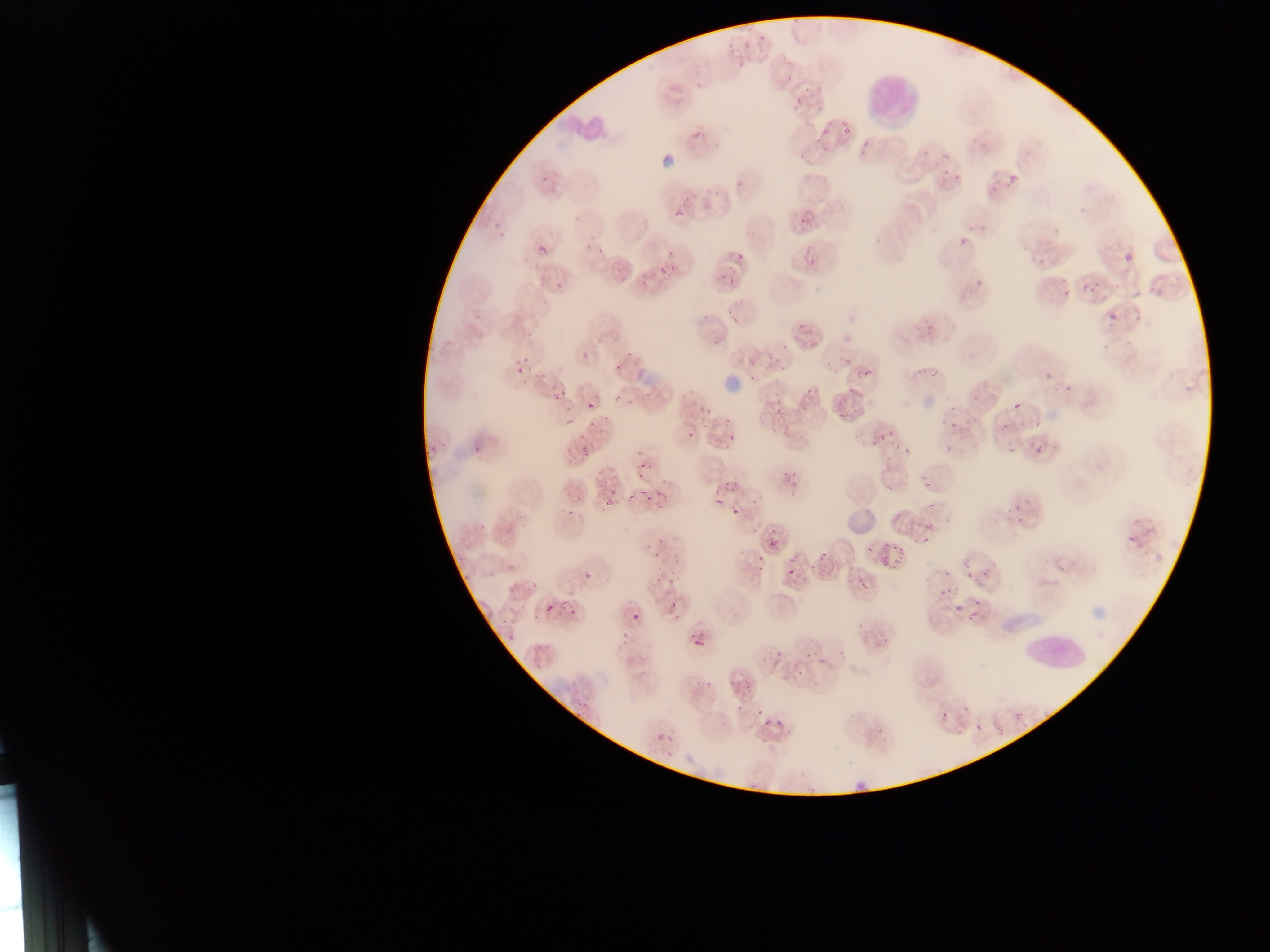
{
  "country": "Ghana",
  "field_of_view": "single",
  "leukocyte_locations": "approximate bounding boxes as {left, top, right, bottom} in pixels: {863, 62, 922, 128}, {545, 102, 611, 145}, {1021, 608, 1087, 678}",
  "malaria_parasite_locations": "approximate bounding boxes as {left, top, right, bottom} in pixels: {695, 83, 703, 91}, {692, 131, 702, 140}, {537, 174, 548, 181}, {1011, 175, 1018, 183}, {735, 180, 749, 189}, {683, 189, 697, 199}, {711, 189, 726, 200}, {699, 197, 713, 211}, {673, 203, 686, 220}, {1080, 207, 1087, 216}, {797, 209, 814, 224}, {486, 214, 505, 228}, {498, 227, 511, 239}, {957, 231, 970, 245}, {538, 242, 548, 257}, {596, 243, 608, 254}, {665, 246, 678, 256}, {805, 247, 817, 256}, {1125, 252, 1133, 263}, {736, 254, 744, 260}, {803, 257, 820, 267}, {1037, 259, 1045, 267}, {670, 261, 680, 279}, {658, 263, 669, 279}, {715, 273, 739, 290}, {555, 274, 566, 289}, {975, 275, 983, 288}, {639, 276, 653, 288}, {1095, 280, 1101, 288}, {1085, 284, 1094, 292}, {1064, 288, 1071, 297}, {1155, 289, 1163, 297}, {726, 307, 736, 316}, {698, 310, 715, 324}, {1108, 310, 1116, 320}, {473, 311, 481, 325}, {731, 315, 740, 325}, {926, 321, 936, 330}, {795, 324, 806, 344}, {527, 329, 534, 338}, {594, 332, 606, 342}, {710, 333, 719, 343}, {809, 337, 823, 346}, {1102, 340, 1111, 351}, {781, 341, 790, 354}, {625, 349, 635, 358}, {582, 350, 593, 364}, {766, 351, 779, 365}, {746, 353, 760, 365}, {520, 354, 529, 363}, {781, 355, 790, 373}, {839, 355, 848, 364}, {914, 363, 928, 376}, {933, 363, 943, 377}, {611, 364, 624, 371}, {524, 367, 534, 373}, {828, 367, 837, 380}, {513, 368, 521, 376}, {533, 368, 549, 382}, {747, 369, 760, 387}, {858, 369, 869, 378}, {775, 371, 786, 384}, {1044, 372, 1052, 380}, {848, 377, 858, 394}, {806, 380, 818, 398}, {1065, 381, 1077, 391}, {1184, 383, 1193, 394}, {550, 385, 571, 402}, {971, 389, 983, 401}, {679, 390, 692, 399}, {610, 393, 621, 405}, {627, 393, 641, 408}, {588, 397, 595, 410}, {948, 402, 958, 413}, {849, 403, 860, 420}, {1013, 403, 1020, 411}, {778, 406, 787, 417}, {563, 407, 574, 414}, {701, 407, 714, 416}, {764, 407, 773, 421}, {836, 409, 846, 418}, {601, 412, 613, 424}, {721, 413, 731, 422}, {964, 414, 974, 425}, {1001, 414, 1010, 433}, {938, 417, 948, 425}, {563, 418, 574, 426}, {948, 418, 959, 431}, {1017, 418, 1031, 427}, {1036, 418, 1044, 428}, {584, 423, 597, 435}, {780, 424, 800, 433}, {881, 425, 895, 441}, {699, 427, 709, 435}, {771, 428, 779, 434}, {686, 430, 695, 440}, {576, 432, 586, 440}, {725, 432, 739, 445}, {440, 433, 446, 449}, {868, 435, 881, 450}, {1034, 439, 1047, 456}, {430, 441, 438, 453}, {723, 441, 733, 450}, {892, 441, 900, 450}, {944, 443, 954, 460}, {473, 444, 485, 453}, {566, 444, 574, 454}, {902, 444, 915, 455}, {1007, 444, 1016, 456}, {581, 446, 591, 456}, {565, 459, 575, 468}, {635, 460, 654, 478}, {882, 462, 890, 478}, {785, 468, 792, 478}, {792, 469, 805, 487}, {917, 474, 927, 482}, {661, 475, 668, 488}, {921, 481, 931, 489}, {726, 482, 742, 494}, {881, 483, 892, 496}, {607, 487, 619, 494}, {713, 487, 722, 500}, {793, 489, 801, 498}, {623, 492, 635, 507}, {573, 494, 586, 502}, {644, 494, 653, 506}, {655, 494, 670, 510}, {924, 494, 936, 509}, {751, 496, 759, 509}, {598, 497, 615, 510}, {714, 497, 725, 507}, {1014, 499, 1024, 513}, {731, 504, 741, 518}, {564, 505, 573, 522}, {892, 506, 903, 522}, {1006, 506, 1013, 518}, {518, 511, 527, 518}, {1017, 513, 1025, 523}, {921, 521, 936, 536}, {1143, 522, 1156, 533}, {478, 523, 489, 532}, {520, 523, 529, 530}, {502, 525, 519, 532}, {751, 526, 759, 535}, {1126, 533, 1134, 542}, {761, 535, 787, 551}, {919, 537, 926, 547}, {880, 538, 894, 555}, {657, 540, 666, 546}, {864, 545, 872, 554}, {891, 546, 908, 559}, {1151, 548, 1164, 559}, {654, 549, 659, 559}, {818, 551, 826, 560}, {788, 552, 796, 562}, {957, 553, 973, 569}, {456, 554, 468, 563}, {751, 555, 764, 566}, {881, 556, 888, 564}, {671, 557, 682, 573}, {890, 558, 900, 571}, {789, 563, 796, 582}, {982, 565, 988, 580}, {506, 566, 514, 574}, {756, 566, 762, 574}, {818, 568, 829, 577}, {966, 568, 975, 585}, {799, 569, 808, 582}, {935, 569, 958, 577}, {462, 572, 470, 581}, {584, 572, 592, 580}, {655, 574, 663, 586}, {668, 577, 680, 585}, {529, 578, 540, 587}, {861, 582, 871, 595}, {507, 586, 516, 595}, {935, 586, 957, 598}, {781, 590, 788, 602}, {669, 599, 679, 616}, {969, 599, 988, 613}, {519, 601, 528, 610}, {546, 602, 556, 613}, {953, 605, 960, 616}, {567, 609, 576, 619}, {530, 611, 541, 621}, {632, 611, 642, 621}, {967, 611, 981, 621}, {925, 616, 939, 623}, {501, 619, 513, 627}, {856, 620, 866, 631}, {621, 628, 634, 646}, {506, 633, 516, 645}, {533, 635, 548, 654}, {879, 635, 892, 643}, {694, 637, 704, 647}, {800, 641, 821, 663}, {838, 647, 843, 660}, {760, 650, 769, 662}, {817, 657, 824, 665}, {798, 667, 808, 678}, {639, 668, 649, 678}, {728, 678, 741, 691}, {812, 678, 823, 691}, {695, 679, 706, 688}, {741, 682, 752, 695}, {572, 692, 585, 706}, {733, 697, 747, 715}, {964, 706, 972, 713}, {758, 709, 767, 726}, {940, 711, 952, 722}, {759, 713, 778, 726}, {774, 713, 788, 728}, {974, 723, 985, 731}, {995, 725, 1004, 735}, {786, 729, 794, 739}, {876, 729, 885, 738}, {657, 731, 664, 747}, {761, 736, 769, 751}, {665, 737, 678, 744}, {663, 752, 672, 761}, {797, 773, 805, 779}, {852, 776, 866, 797}, {747, 783, 758, 794} | approximate {x, y} pixel centers of objects too small to bound: {736, 262}, {790, 441}, {1058, 445}, {770, 526}, {491, 576}, {564, 603}, {731, 617}, {777, 654}, {1018, 715}, {580, 716}",
  "preparation": "thin blood smear",
  "image_size": "1270×952 pixels",
  "capture": "mobile-phone photograph through a microscope"
}